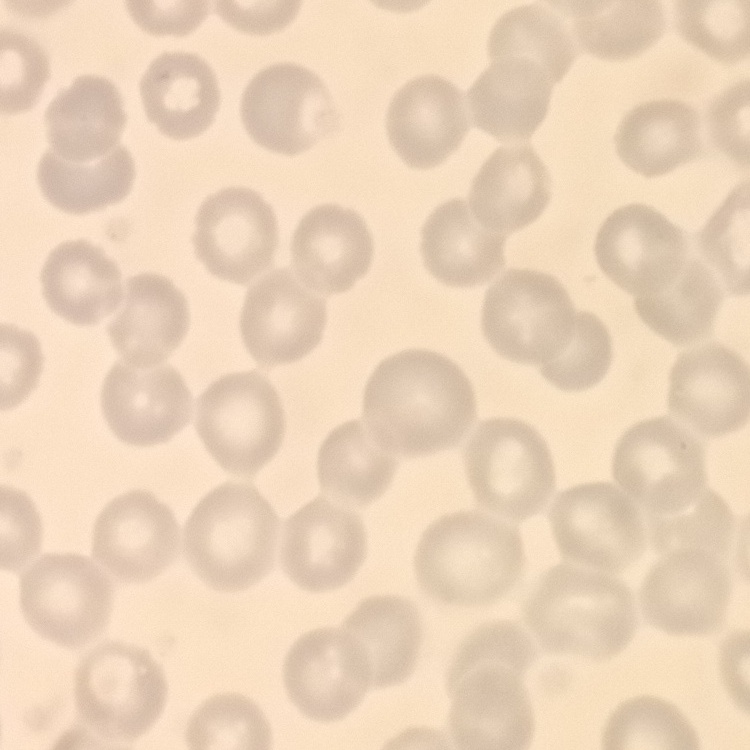
Summary:
  - Erythrocyte morphology: no rouleaux formation
  - Preparation: thin blood film
  - Image type: square crop of a larger photomicrograph
  - Stain: Field's or Giemsa